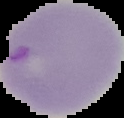

Summary:
  - Image size: 124×118 pixels
  - Image type: segmented cell region with the area outside set to black
  - Result: malaria parasites detected
  - Preparation: thin blood film